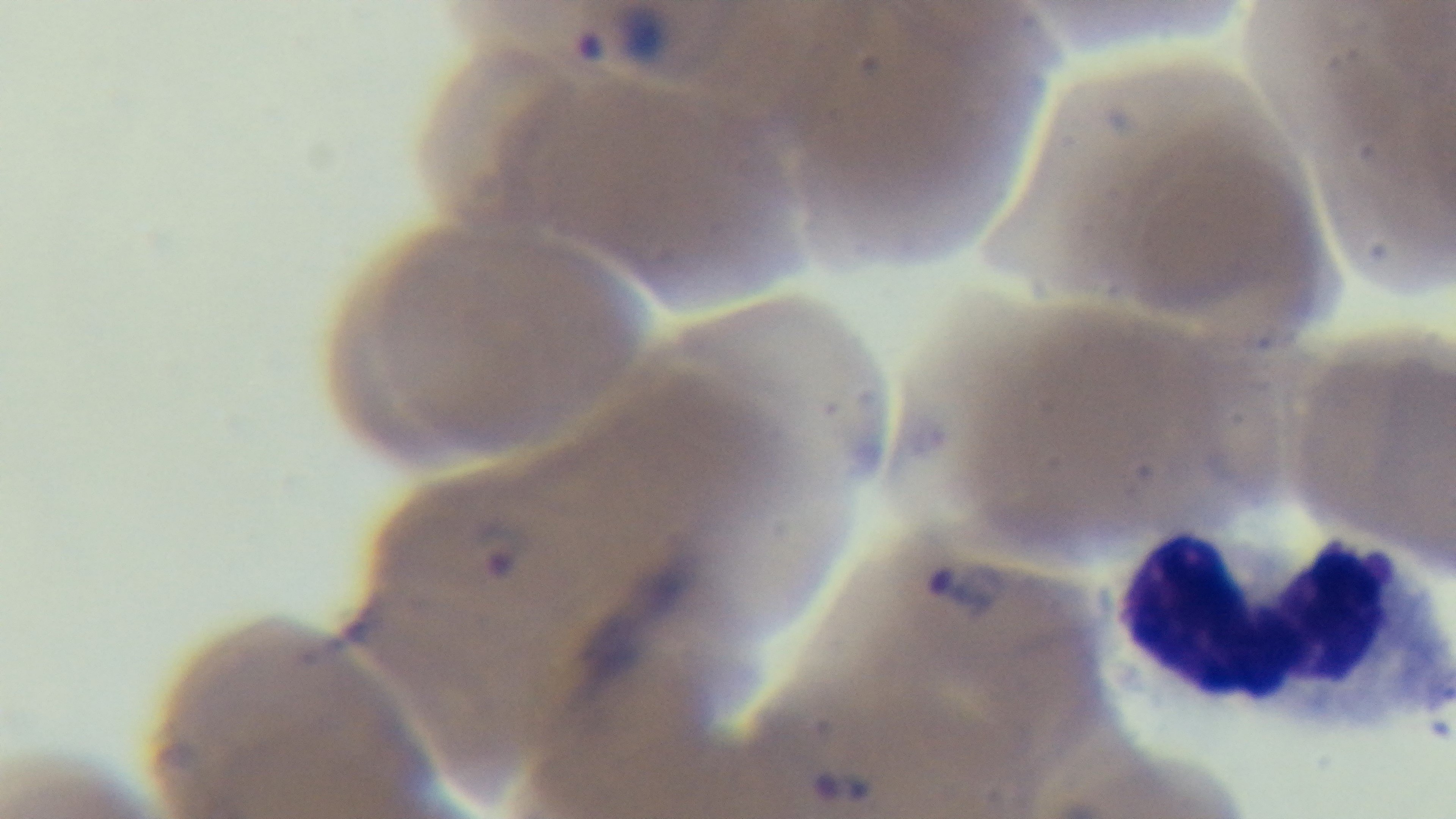

Summary:
  - Modality: light microscopy
  - Stain: Giemsa
  - Field of view: single
  - Malaria status: infected
  - Preparation: thin
  - Objective: 100x oil immersion
  - Capture: mounted 4K digital camera